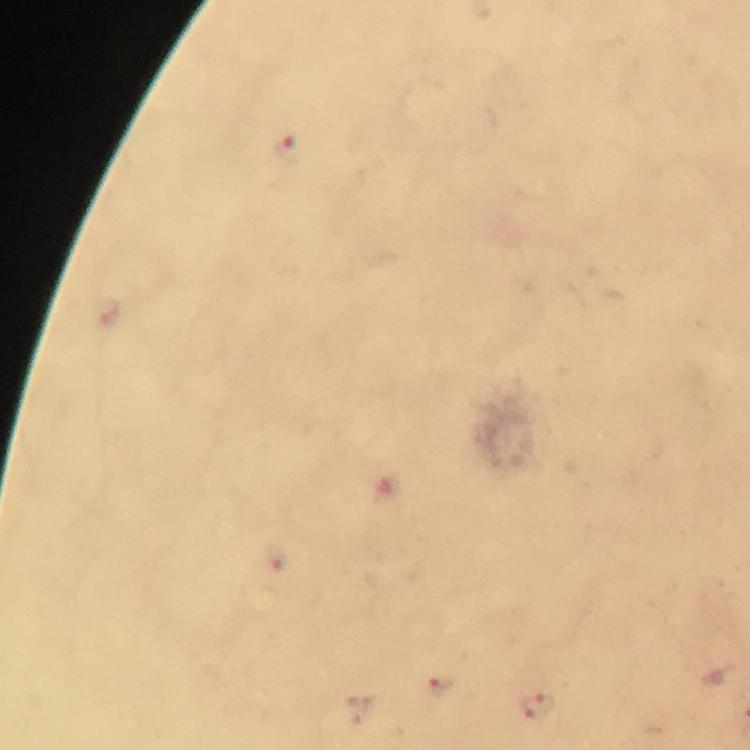

context = from a diagnostic examination for malaria
image size = 750×750 pixels
Plasmodium parasite locations = approximate centers as (x, y) in pixels: (288, 150), (442, 688), (538, 709)
capture = smartphone camera through the microscope
cropped from = one field of view
immersion oil = applied
stain = Giemsa
preparation = thick smear
magnification = 100x